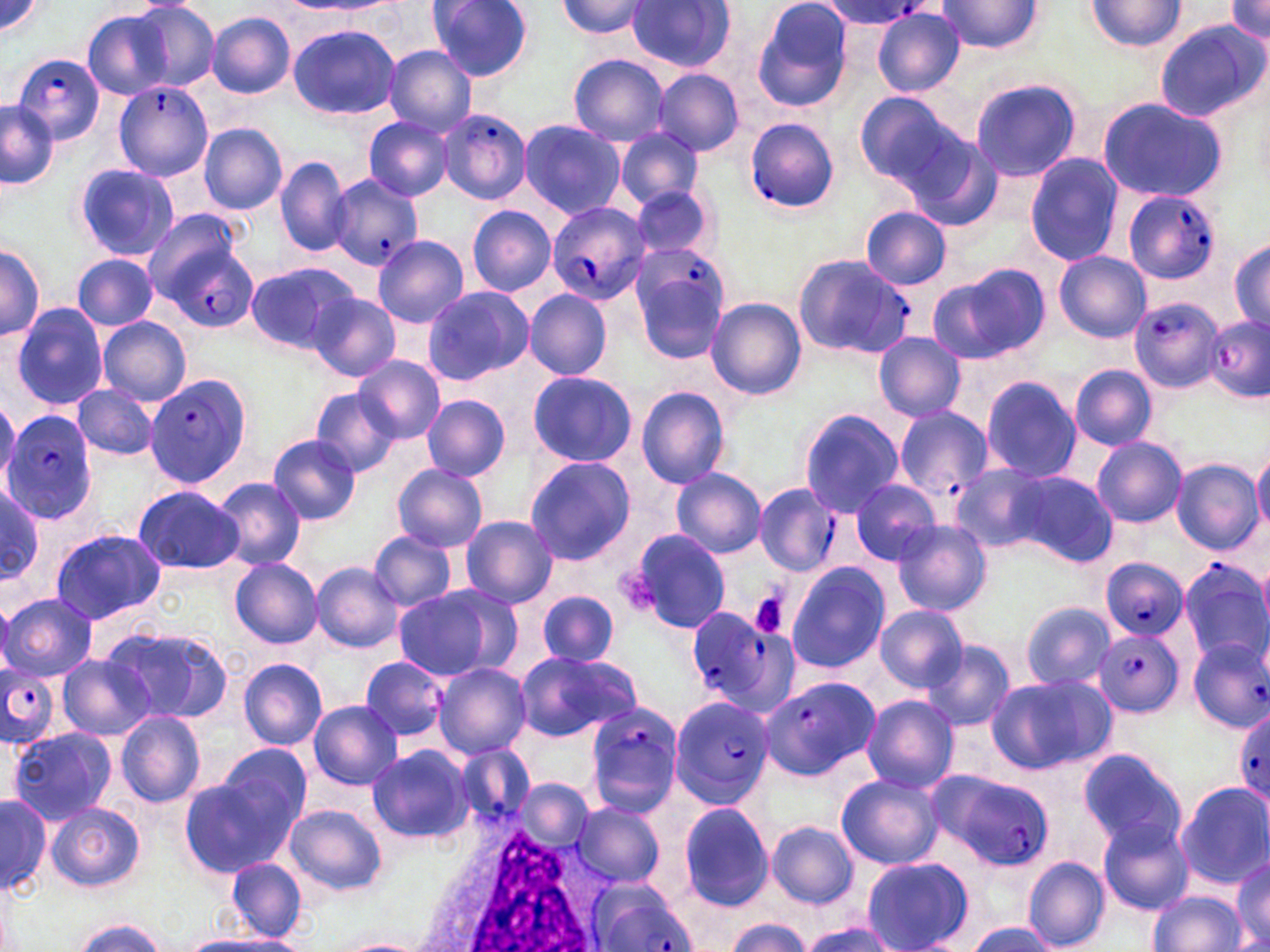 Approximate bounding boxes as named x1/y1/x2/y2 corners in pixels. Plasmodium falciparum-infected red blood cell locations: (x1=817, y1=1, x2=934, y2=29), (x1=12, y1=54, x2=104, y2=146), (x1=114, y1=80, x2=214, y2=182), (x1=439, y1=106, x2=530, y2=204), (x1=743, y1=116, x2=841, y2=213), (x1=327, y1=175, x2=423, y2=273), (x1=1122, y1=189, x2=1222, y2=285), (x1=545, y1=201, x2=647, y2=304), (x1=149, y1=222, x2=256, y2=329), (x1=625, y1=242, x2=730, y2=362), (x1=792, y1=253, x2=912, y2=359), (x1=1129, y1=295, x2=1222, y2=393), (x1=1202, y1=316, x2=1269, y2=401), (x1=147, y1=375, x2=252, y2=490), (x1=891, y1=405, x2=994, y2=506), (x1=3, y1=409, x2=100, y2=523), (x1=755, y1=484, x2=843, y2=577), (x1=1098, y1=558, x2=1190, y2=638), (x1=1184, y1=559, x2=1267, y2=668), (x1=685, y1=609, x2=797, y2=715), (x1=1095, y1=629, x2=1182, y2=717), (x1=1188, y1=639, x2=1269, y2=733), (x1=0, y1=663, x2=59, y2=747), (x1=759, y1=678, x2=879, y2=779), (x1=669, y1=693, x2=777, y2=808), (x1=583, y1=700, x2=684, y2=814), (x1=1234, y1=703, x2=1269, y2=811), (x1=454, y1=742, x2=534, y2=828), (x1=934, y1=768, x2=1053, y2=868), (x1=585, y1=879, x2=696, y2=952). Platelet locations: (x1=615, y1=566, x2=666, y2=614), (x1=747, y1=592, x2=790, y2=640). White blood cell locations: (x1=420, y1=812, x2=617, y2=951). Uninfected red blood cell locations: (x1=1, y1=0, x2=47, y2=43), (x1=427, y1=0, x2=534, y2=82), (x1=752, y1=0, x2=855, y2=113), (x1=555, y1=1, x2=654, y2=40), (x1=628, y1=1, x2=735, y2=73), (x1=935, y1=1, x2=1045, y2=54), (x1=1086, y1=1, x2=1186, y2=51), (x1=1226, y1=1, x2=1270, y2=47), (x1=129, y1=2, x2=220, y2=92), (x1=872, y1=7, x2=965, y2=97), (x1=83, y1=10, x2=173, y2=99), (x1=207, y1=12, x2=295, y2=98), (x1=1153, y1=18, x2=1268, y2=122), (x1=288, y1=24, x2=401, y2=121), (x1=383, y1=47, x2=476, y2=135), (x1=568, y1=54, x2=670, y2=146), (x1=655, y1=68, x2=743, y2=156), (x1=968, y1=75, x2=1083, y2=182), (x1=853, y1=90, x2=963, y2=192), (x1=1095, y1=96, x2=1229, y2=204), (x1=1, y1=100, x2=58, y2=188), (x1=364, y1=118, x2=453, y2=200), (x1=517, y1=119, x2=626, y2=220), (x1=200, y1=123, x2=288, y2=214), (x1=614, y1=128, x2=704, y2=209), (x1=905, y1=130, x2=1005, y2=232), (x1=1024, y1=153, x2=1122, y2=266), (x1=276, y1=155, x2=350, y2=257), (x1=74, y1=161, x2=179, y2=262), (x1=629, y1=184, x2=717, y2=263), (x1=467, y1=205, x2=557, y2=296), (x1=860, y1=207, x2=951, y2=288), (x1=372, y1=235, x2=469, y2=328), (x1=1230, y1=240, x2=1269, y2=330), (x1=0, y1=243, x2=44, y2=341), (x1=1055, y1=251, x2=1151, y2=342), (x1=72, y1=254, x2=158, y2=330), (x1=244, y1=261, x2=355, y2=356), (x1=934, y1=263, x2=1052, y2=364), (x1=422, y1=285, x2=534, y2=384), (x1=524, y1=290, x2=610, y2=381), (x1=307, y1=292, x2=401, y2=383), (x1=706, y1=298, x2=806, y2=399), (x1=10, y1=302, x2=109, y2=411), (x1=99, y1=316, x2=191, y2=404), (x1=874, y1=332, x2=965, y2=421), (x1=353, y1=356, x2=445, y2=444), (x1=1070, y1=364, x2=1157, y2=450), (x1=527, y1=371, x2=638, y2=468), (x1=980, y1=376, x2=1082, y2=483), (x1=73, y1=385, x2=158, y2=460), (x1=637, y1=387, x2=732, y2=489), (x1=309, y1=388, x2=402, y2=478), (x1=420, y1=393, x2=511, y2=482), (x1=798, y1=409, x2=904, y2=516), (x1=267, y1=435, x2=361, y2=525), (x1=1091, y1=437, x2=1188, y2=527), (x1=1252, y1=450, x2=1270, y2=534), (x1=523, y1=455, x2=636, y2=566), (x1=1171, y1=459, x2=1262, y2=555), (x1=950, y1=463, x2=1054, y2=553), (x1=392, y1=465, x2=488, y2=552), (x1=671, y1=468, x2=767, y2=558), (x1=1006, y1=472, x2=1117, y2=567), (x1=211, y1=476, x2=308, y2=571), (x1=850, y1=478, x2=943, y2=566), (x1=0, y1=484, x2=45, y2=585), (x1=133, y1=484, x2=244, y2=576), (x1=460, y1=515, x2=558, y2=610), (x1=892, y1=521, x2=991, y2=616), (x1=49, y1=528, x2=166, y2=625), (x1=626, y1=529, x2=731, y2=633), (x1=368, y1=532, x2=458, y2=611), (x1=228, y1=558, x2=323, y2=648), (x1=309, y1=561, x2=404, y2=653), (x1=785, y1=563, x2=890, y2=672), (x1=393, y1=584, x2=519, y2=681), (x1=536, y1=590, x2=618, y2=667), (x1=1, y1=593, x2=96, y2=681), (x1=1022, y1=601, x2=1115, y2=692), (x1=874, y1=605, x2=969, y2=692), (x1=108, y1=626, x2=236, y2=725), (x1=919, y1=638, x2=1016, y2=732), (x1=513, y1=649, x2=640, y2=741), (x1=57, y1=655, x2=155, y2=740), (x1=359, y1=657, x2=448, y2=742), (x1=239, y1=659, x2=327, y2=750), (x1=326, y1=660, x2=445, y2=786), (x1=434, y1=661, x2=531, y2=760), (x1=988, y1=672, x2=1116, y2=774), (x1=862, y1=695, x2=959, y2=792), (x1=308, y1=699, x2=403, y2=790), (x1=117, y1=710, x2=207, y2=807), (x1=6, y1=727, x2=116, y2=825), (x1=216, y1=741, x2=312, y2=837), (x1=366, y1=744, x2=474, y2=845), (x1=1078, y1=748, x2=1186, y2=851), (x1=836, y1=773, x2=943, y2=870), (x1=178, y1=775, x2=292, y2=878), (x1=517, y1=778, x2=592, y2=852), (x1=1177, y1=781, x2=1270, y2=888), (x1=1, y1=791, x2=52, y2=895), (x1=48, y1=801, x2=144, y2=893), (x1=572, y1=801, x2=664, y2=887), (x1=677, y1=802, x2=773, y2=910), (x1=284, y1=805, x2=387, y2=897), (x1=1099, y1=818, x2=1193, y2=914), (x1=766, y1=821, x2=859, y2=908), (x1=861, y1=855, x2=974, y2=952), (x1=1231, y1=855, x2=1270, y2=948), (x1=1025, y1=856, x2=1111, y2=950), (x1=228, y1=857, x2=307, y2=941), (x1=1150, y1=891, x2=1246, y2=952), (x1=723, y1=918, x2=816, y2=952), (x1=801, y1=919, x2=899, y2=952), (x1=71, y1=920, x2=169, y2=952), (x1=965, y1=922, x2=1055, y2=952), (x1=182, y1=933, x2=307, y2=952), (x1=335, y1=937, x2=432, y2=952). Slide-level diagnosis: Plasmodium falciparum. 1000x magnification. Image is 1270×952 pixels. May-Grünwald-Giemsa stain. One field of a larger specimen. Optical microscopy. Thin blood smear.